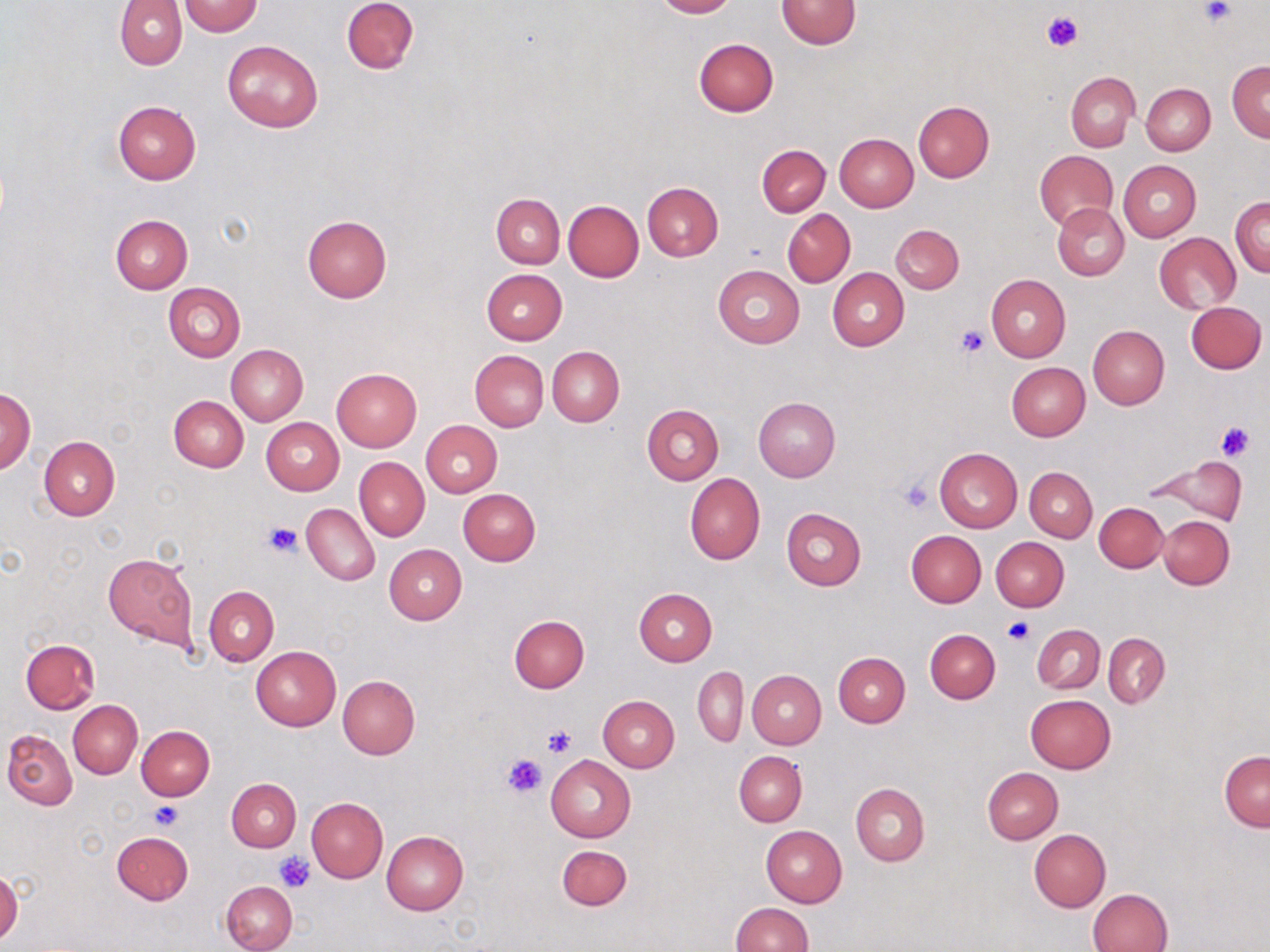
Approximate bounding boxes as [x1, y1, x2, y2] in pixels. Platelet locations: [1202, 1, 1233, 24], [1043, 10, 1082, 52], [956, 325, 988, 359], [1214, 420, 1255, 460], [897, 476, 936, 514], [265, 520, 302, 557], [1002, 616, 1033, 645], [544, 725, 575, 757], [502, 752, 549, 797], [150, 802, 182, 830], [275, 851, 314, 892]. Uninfected red blood cell locations: [341, 0, 418, 74], [653, 0, 736, 18], [776, 0, 860, 49], [114, 1, 187, 69], [179, 1, 263, 36], [693, 38, 778, 116], [222, 40, 324, 132], [1227, 59, 1270, 142], [1067, 72, 1138, 152], [1141, 83, 1215, 155], [113, 100, 200, 184], [913, 100, 994, 182], [834, 133, 918, 211], [757, 144, 830, 217], [1035, 149, 1119, 230], [1118, 160, 1201, 242], [643, 181, 724, 261], [491, 193, 565, 268], [1231, 195, 1270, 278], [563, 201, 644, 282], [1053, 204, 1129, 280], [783, 209, 855, 286], [111, 215, 192, 294], [302, 215, 391, 303], [891, 224, 964, 294], [1153, 233, 1241, 312], [712, 266, 805, 348], [828, 267, 909, 350], [480, 269, 567, 345], [986, 274, 1070, 362], [162, 282, 244, 362], [1187, 301, 1265, 373], [1088, 325, 1169, 409], [226, 344, 307, 425], [547, 346, 623, 426], [469, 350, 549, 431], [1006, 363, 1091, 440], [331, 368, 422, 451], [1, 387, 36, 475], [169, 396, 248, 472], [754, 398, 840, 482], [642, 404, 724, 484], [261, 417, 345, 495], [421, 420, 502, 497], [39, 435, 120, 519], [935, 448, 1023, 532], [1145, 454, 1246, 525], [355, 457, 429, 540], [1025, 467, 1096, 541], [684, 472, 765, 565], [457, 488, 541, 565], [1094, 502, 1168, 572], [302, 503, 380, 586], [781, 508, 866, 590], [1158, 516, 1234, 589], [906, 530, 986, 607], [991, 537, 1069, 611], [384, 544, 467, 624], [103, 553, 198, 651], [205, 587, 279, 664], [634, 588, 718, 666], [509, 615, 589, 692], [1033, 625, 1104, 693], [925, 629, 1000, 703], [1104, 633, 1169, 708], [20, 639, 101, 714], [251, 646, 340, 730], [833, 653, 910, 727], [693, 667, 747, 746], [748, 670, 826, 748], [337, 676, 419, 760], [1026, 694, 1115, 773], [598, 695, 679, 772], [68, 700, 143, 778], [137, 725, 215, 800], [3, 728, 78, 809], [734, 751, 806, 827], [1219, 751, 1269, 831], [545, 754, 635, 842], [982, 767, 1063, 844], [227, 777, 301, 852], [851, 784, 929, 866], [306, 797, 387, 882], [761, 825, 848, 907], [1028, 828, 1111, 912], [112, 831, 194, 905], [382, 831, 469, 915], [556, 844, 631, 911], [0, 868, 23, 945], [222, 880, 297, 952], [1089, 888, 1173, 952], [730, 903, 812, 951]. Slide-level diagnosis: negative for blood parasites. May-Grünwald-Giemsa stain. Image is 1270×952 pixels. Captured at 1000x magnification. Optical microscopy. Thin blood smear. Single field of view.